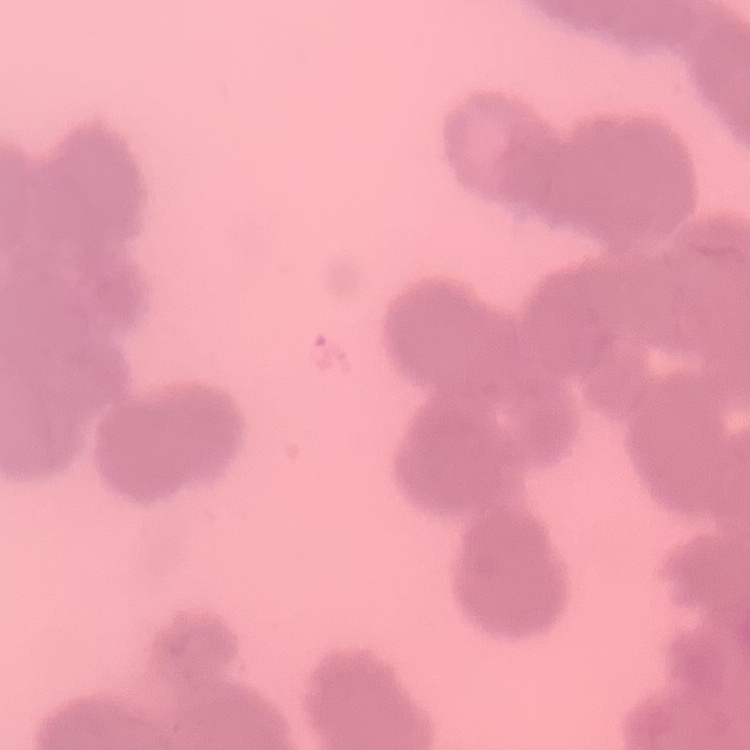

The red blood cells show rouleaux formation. Field's or Giemsa stain. Square crop of a larger photomicrograph. Thin blood film.